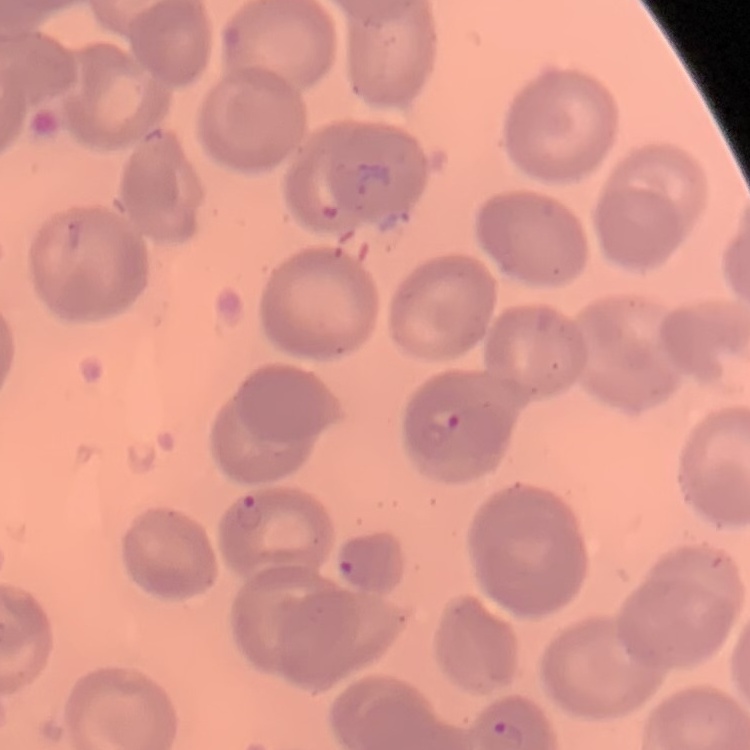
red blood cell morphology = no rouleaux formation
stain = Field's or Giemsa
image type = square crop of a larger photomicrograph
preparation = thin blood smear